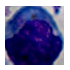
{
  "magnification": "1000x",
  "identification": "leukocyte",
  "modality": "photomicrograph"
}